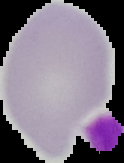
Summary:
  - Preparation: thin blood smear
  - Image size: 124×163 pixels
  - Image type: segmented cell region with the area outside set to black
  - Malaria status: uninfected